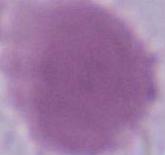 An erythrocyte is seen. 1000x magnification. Micrograph.